Point out each Plasmodium parasite.
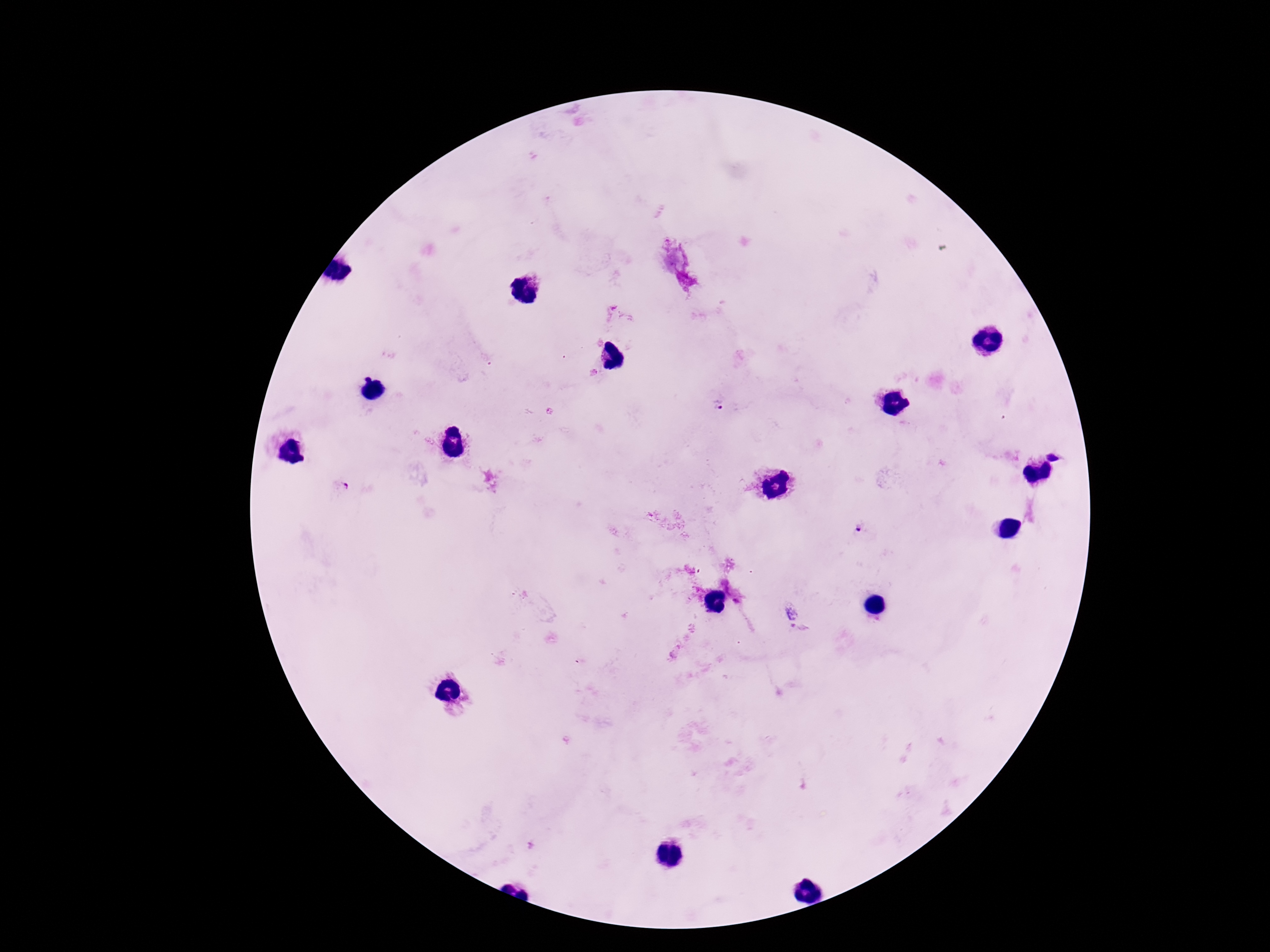

Approximate object centers, in pixels from the top-left corner.
Plasmodium parasites: (x=593, y=373), (x=718, y=406), (x=549, y=411), (x=1054, y=454), (x=342, y=486), (x=859, y=529), (x=791, y=613), (x=793, y=625).

Smartphone photograph taken through the microscope eyepiece. Patient malaria status: positive. Thick blood smear. Image is 1270×952 pixels. One field from this slide. Giemsa stain. 100x magnification.